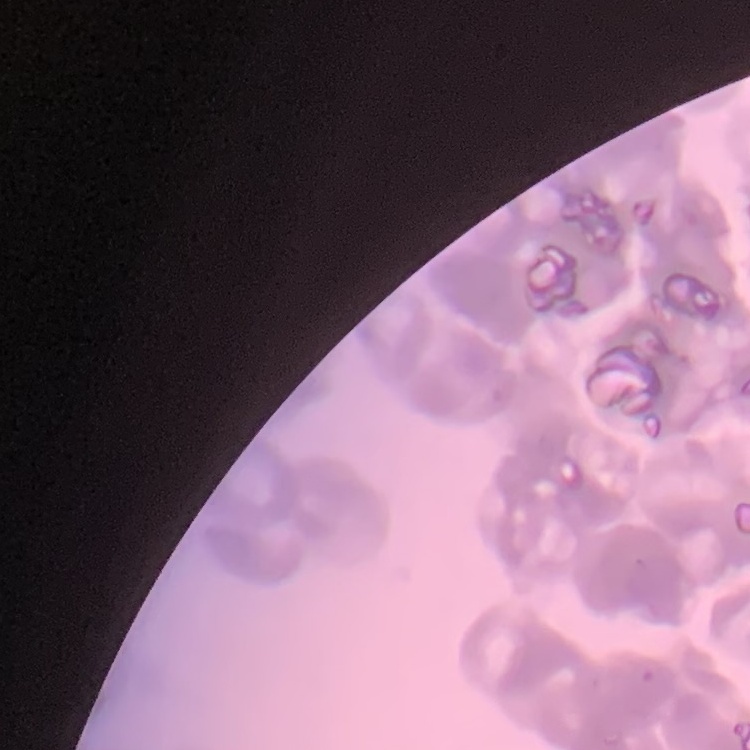

erythrocyte morphology = rouleaux formation
preparation = thin peripheral smear
stain = Field's or Giemsa
image type = square crop of a larger photomicrograph